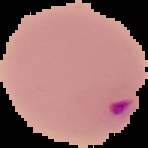 Segmented cell region on a black background. From a thin blood film. Image is 148×148 pixels. Malaria status: parasitized.